Identify the parasite.
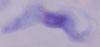

This is a trypanosome.

Captured at 1000x magnification. Micrograph.